Mark where leukocytes are.
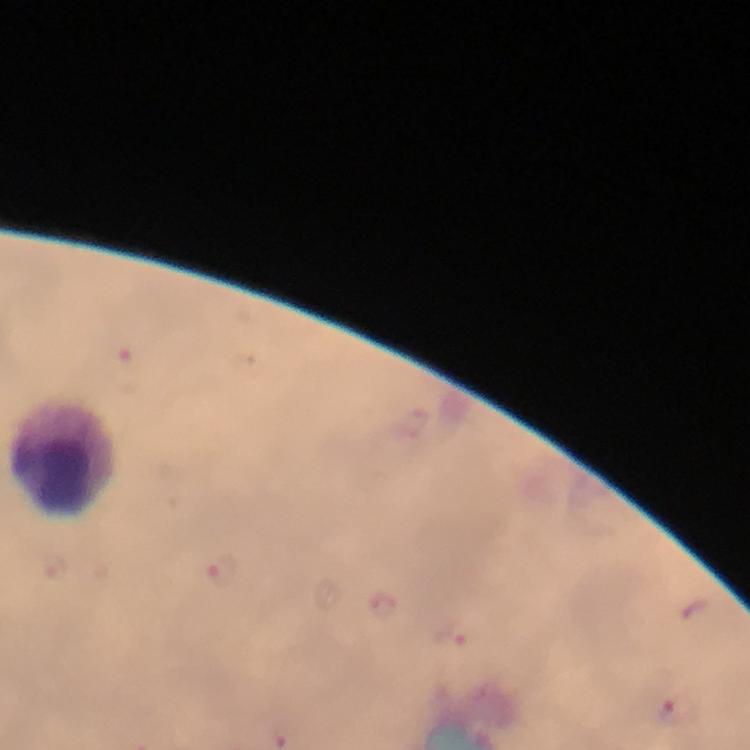
Approximate centers as [x, y] in pixels.
Leukocytes: [70, 457].

preparation = thick blood film
stain = Giemsa
immersion oil = used
malaria parasite locations = approximate centers as [x, y] in pixels: [223, 575], [381, 607], [457, 638], [680, 710]
image size = 750×750 pixels
context = from a malaria diagnostic workup
cropped from = a single field of view
magnification = 100x
capture = smartphone mounted on the microscope